Locate every uninfected red blood cell.
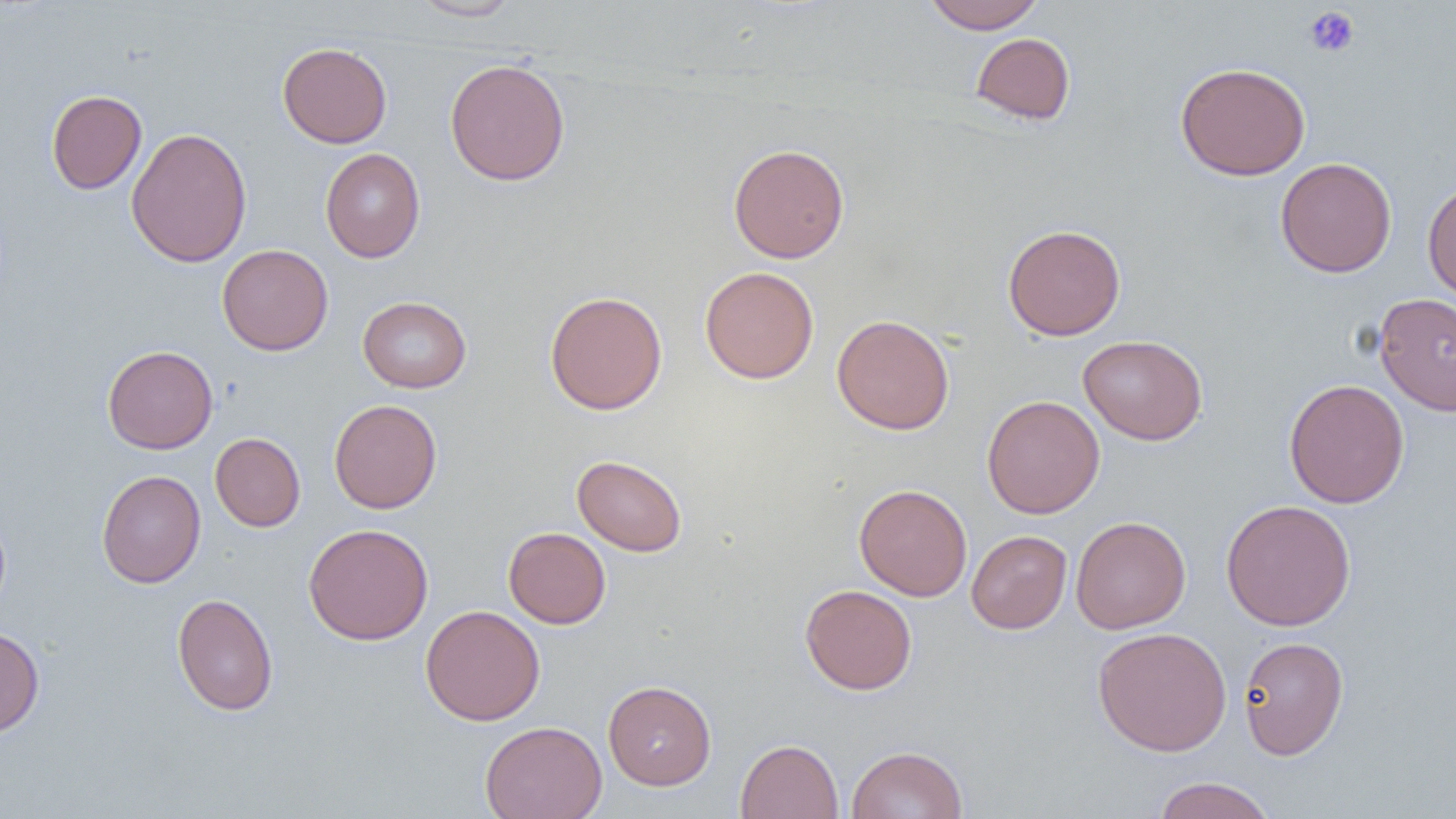

Approximate bounding boxes as (x1,y1)-(x2,y2) corner pairs in pixels.
Uninfected red blood cells: (408,0)-(521,21), (923,0)-(1045,34), (971,32)-(1076,125), (277,42)-(392,148), (444,58)-(570,185), (1175,61)-(1311,181), (46,89)-(147,194), (126,126)-(252,267), (728,143)-(850,263), (320,148)-(425,262), (1275,157)-(1397,278), (1422,180)-(1456,302), (1002,224)-(1126,340), (217,244)-(333,355), (699,266)-(819,384), (544,290)-(667,415), (1374,293)-(1456,416), (357,295)-(471,393), (831,314)-(955,434), (1078,334)-(1208,444), (102,345)-(218,454), (1283,379)-(1410,508), (981,395)-(1105,518), (329,399)-(442,513), (210,432)-(306,532), (571,454)-(688,557), (96,469)-(206,588), (853,483)-(972,601), (1221,499)-(1356,631), (0,511)-(11,618), (1070,516)-(1191,634), (303,523)-(434,645), (503,527)-(611,628), (966,530)-(1072,634), (800,584)-(917,695), (172,593)-(278,716), (420,605)-(545,725), (0,626)-(44,737), (1092,626)-(1232,757), (1238,635)-(1349,760), (603,680)-(716,790), (479,721)-(608,819), (735,738)-(843,819), (846,745)-(968,819), (1152,776)-(1277,819).

slide_level_diagnosis: negative for blood parasites
preparation: thin blood smear
modality: light microscopy
field_of_view: single
platelet_locations: 'approximate bounding boxes as (x1,y1)-(x2,y2) corner pairs in pixels: (1304,6)-(1360,58)'
image_size: 1456×819 pixels
magnification: 1000x